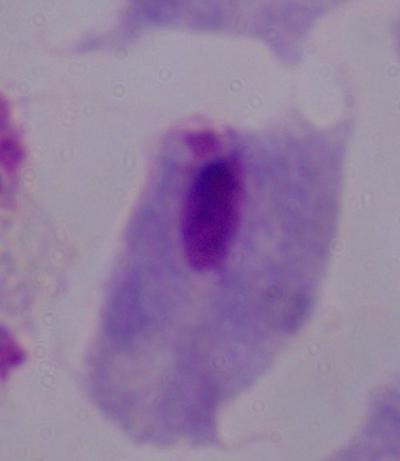
Summary:
  - Magnification: 1000x
  - Identification: trichomonad
  - Modality: micrograph